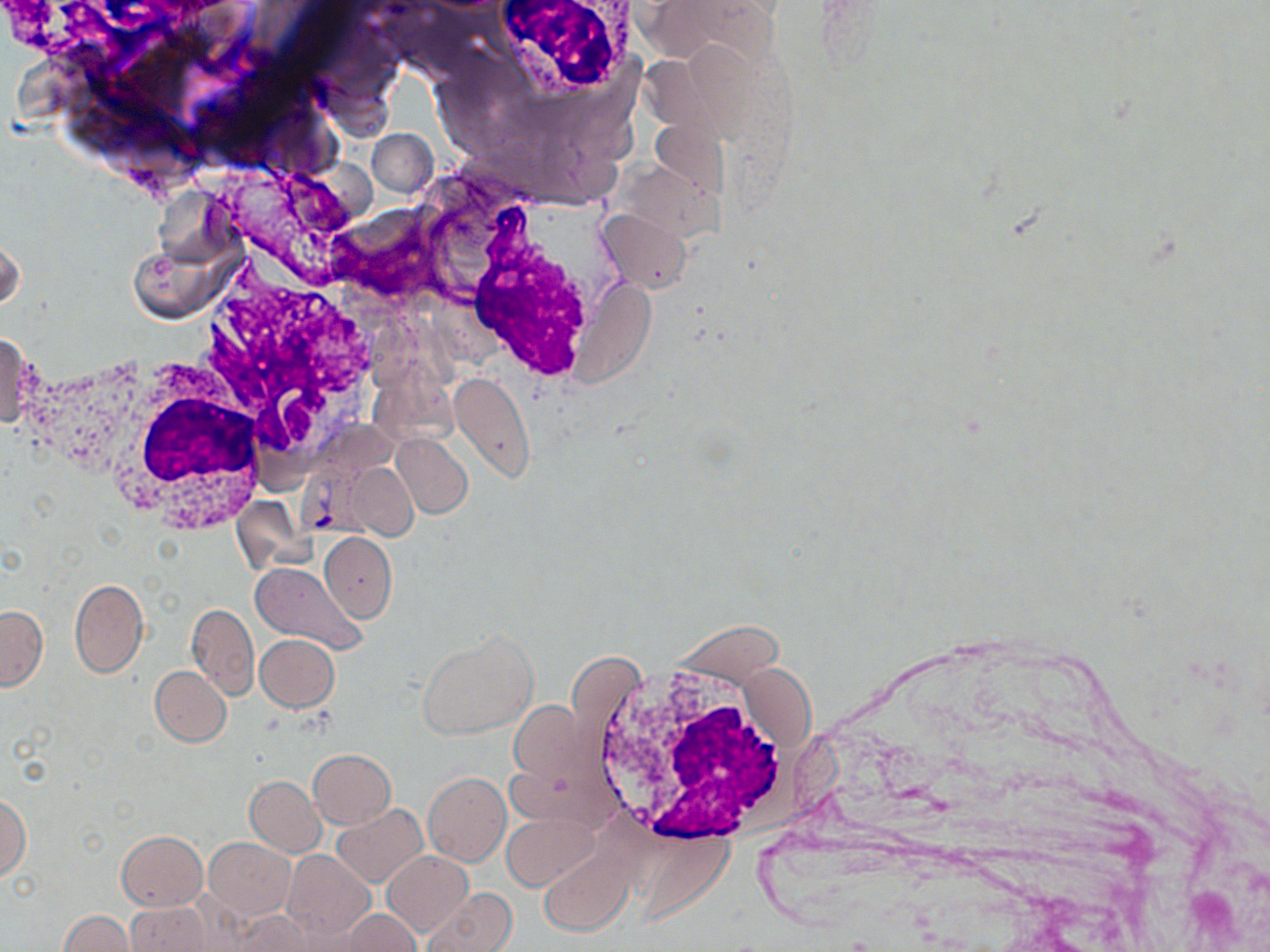
Approximate bounding boxes as (x1,y1)-(x2,y2) corner pairs in pixels. Plasmodium vivax-infected red blood cell locations: (293,463)-(392,536). White blood cell locations: (492,0)-(637,99), (455,211)-(604,387), (194,263)-(381,469), (99,363)-(274,532), (585,658)-(804,847). Uninfected red blood cell locations: (367,129)-(439,197), (597,210)-(692,293), (0,234)-(23,317), (129,244)-(222,322), (0,333)-(37,429), (448,372)-(536,484), (394,435)-(472,517), (348,464)-(419,539), (319,532)-(397,622), (248,561)-(366,652), (69,577)-(147,678), (188,604)-(258,698), (0,605)-(47,691), (418,633)-(536,738), (254,634)-(339,712), (150,665)-(231,747), (511,701)-(587,786), (308,749)-(396,829), (423,772)-(510,867), (245,776)-(326,857), (0,795)-(30,879), (332,803)-(428,886), (504,811)-(599,889), (117,830)-(208,909), (204,837)-(296,919), (539,847)-(635,934), (381,849)-(473,937), (282,850)-(374,941), (422,887)-(517,952), (125,901)-(213,952), (338,909)-(422,951), (60,911)-(135,951), (234,913)-(323,951). Slide-level diagnosis: Plasmodium vivax. May-Grünwald-Giemsa stain. Thin blood film. Light microscopy. Image is 1270×952 pixels. Single field of view. Captured at 1000x magnification.